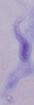
Summary:
  - Modality: micrograph
  - Identification: trypanosome
  - Magnification: 1000x